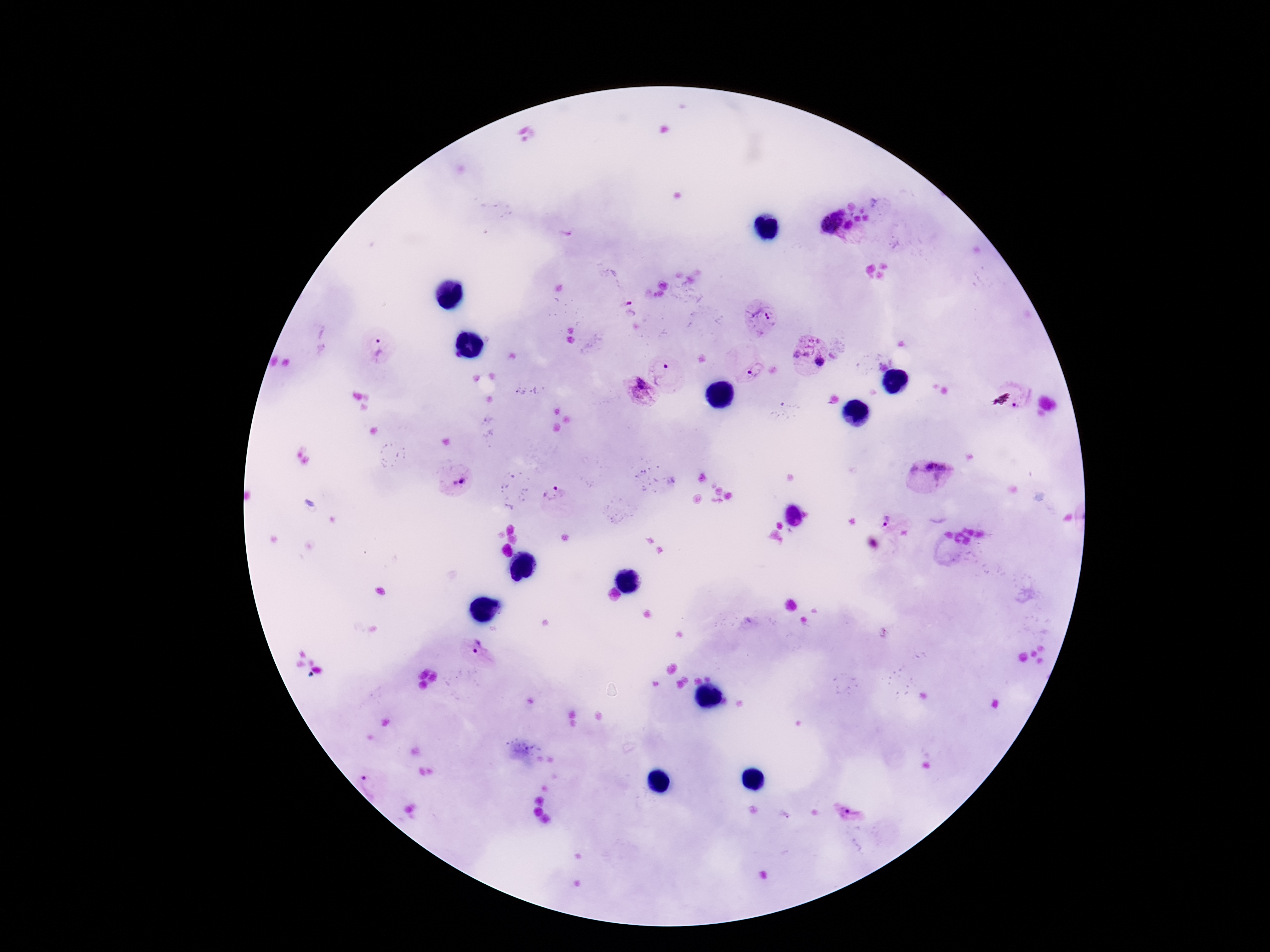

image size = 1270×952 pixels
stain = Giemsa
patient malaria status = infected
Plasmodium parasite locations = approximate centers as {x, y} in pixels: {827, 219}, {850, 226}, {629, 308}, {761, 314}, {804, 340}, {379, 345}, {821, 363}, {753, 370}, {663, 371}, {636, 390}, {1024, 400}, {930, 471}, {461, 479}, {553, 494}, {885, 519}, {476, 646}, {370, 785}, {850, 809}
preparation = thick peripheral-blood smear
field of view = one from this slide
magnification = 100x
capture = smartphone camera through the microscope eyepiece